Point out each leukocyte.
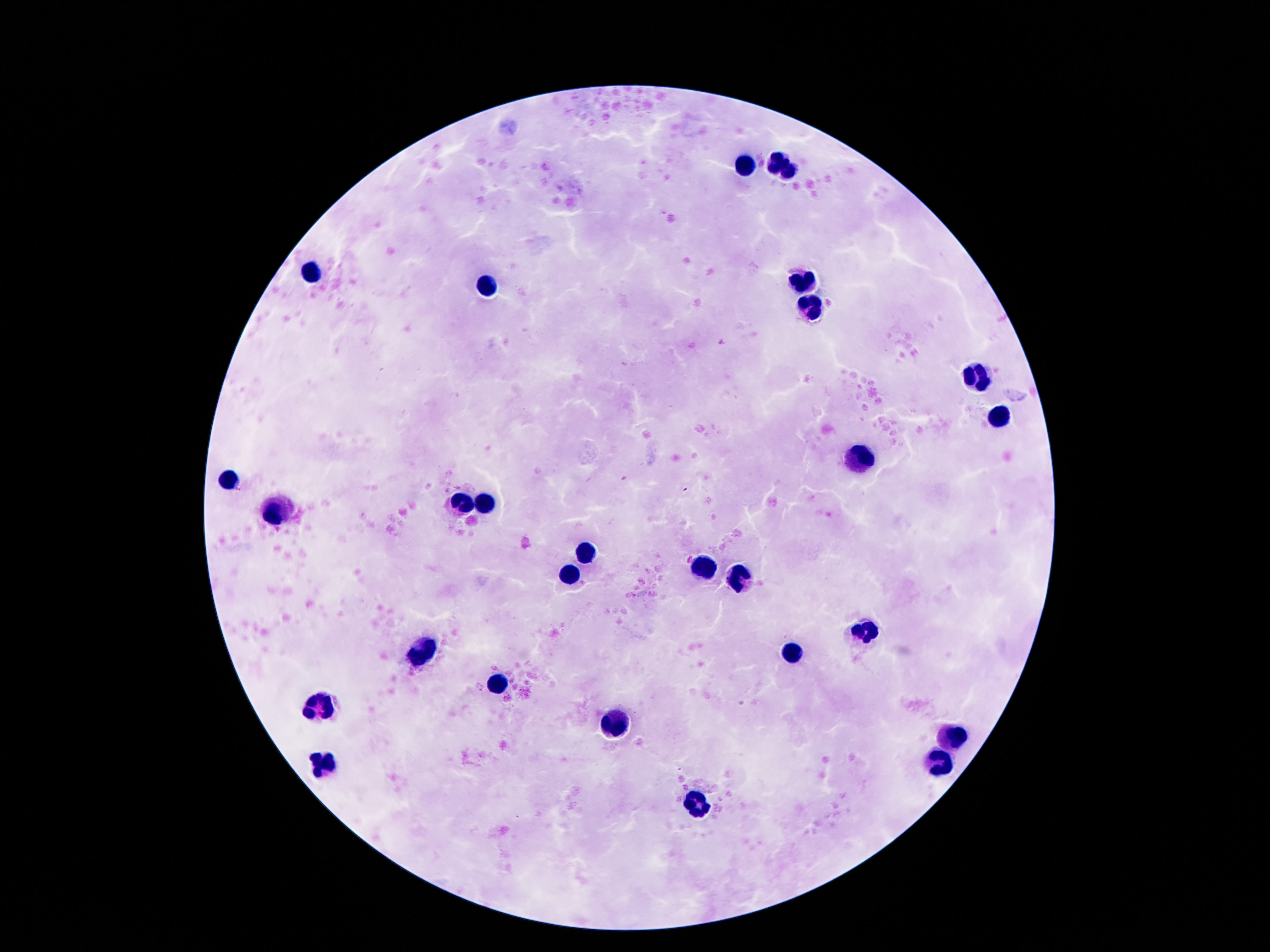

Approximate centers as (x, y) in pixels.
Leukocytes: (776, 160), (746, 169), (790, 173), (310, 270), (806, 283), (486, 286), (812, 307), (975, 377), (998, 417), (862, 463), (228, 480), (457, 500), (488, 503), (279, 511), (587, 553), (702, 568), (572, 574), (736, 576), (866, 627), (423, 652), (795, 654), (495, 685), (321, 704), (614, 728), (956, 736), (325, 763), (940, 763), (700, 804).

Summary:
  - Field of view: one from this slide
  - Magnification: 100x
  - Stain: Giemsa
  - Patient malaria status: uninfected
  - Capture: smartphone camera through the microscope eyepiece
  - Image size: 1270×952 pixels
  - Preparation: thick blood film